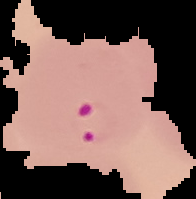

Summary:
  - Preparation: thin blood film
  - Image size: 196×199 pixels
  - Malaria status: parasitized
  - Image type: segmented cell region with the area outside set to black